Locate every leukocyte (white blood cell).
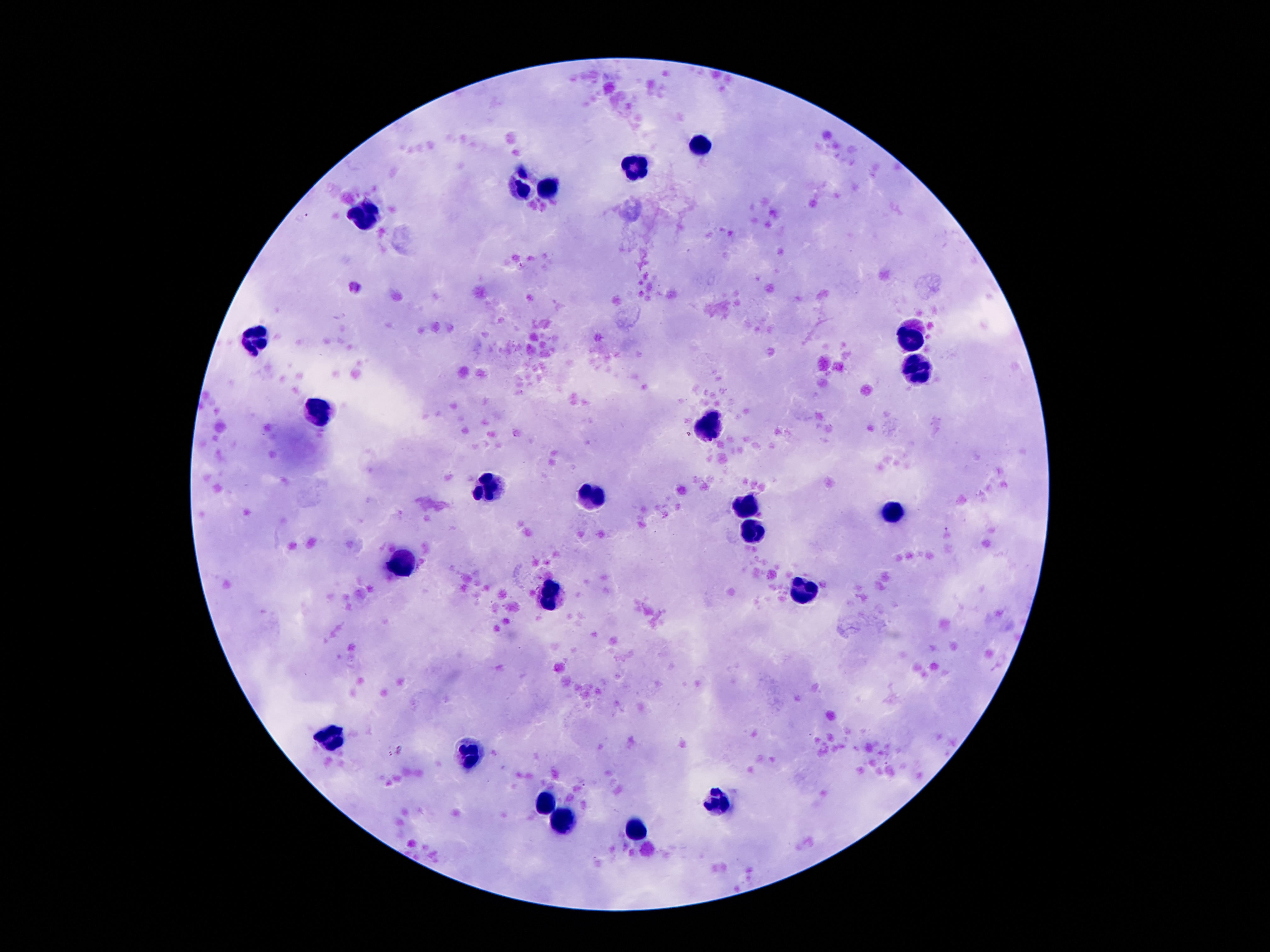
Approximate object centers, in pixels from the top-left corner.
Leukocytes: (x=698, y=146), (x=634, y=169), (x=550, y=190), (x=522, y=191), (x=359, y=210), (x=911, y=334), (x=258, y=339), (x=918, y=367), (x=322, y=413), (x=713, y=432), (x=488, y=489), (x=597, y=500), (x=747, y=507), (x=891, y=515), (x=750, y=530), (x=399, y=562), (x=802, y=591), (x=547, y=606), (x=328, y=738), (x=474, y=755), (x=719, y=802), (x=546, y=804), (x=568, y=822), (x=639, y=831).

Giemsa stain. One field from this slide. Patient malaria status: not infected. Thick peripheral-blood smear. Image is 1270×952 pixels. 100x magnification. Smartphone photograph taken through the microscope eyepiece.